Give the position of every malaria parasite and every leukocyte.
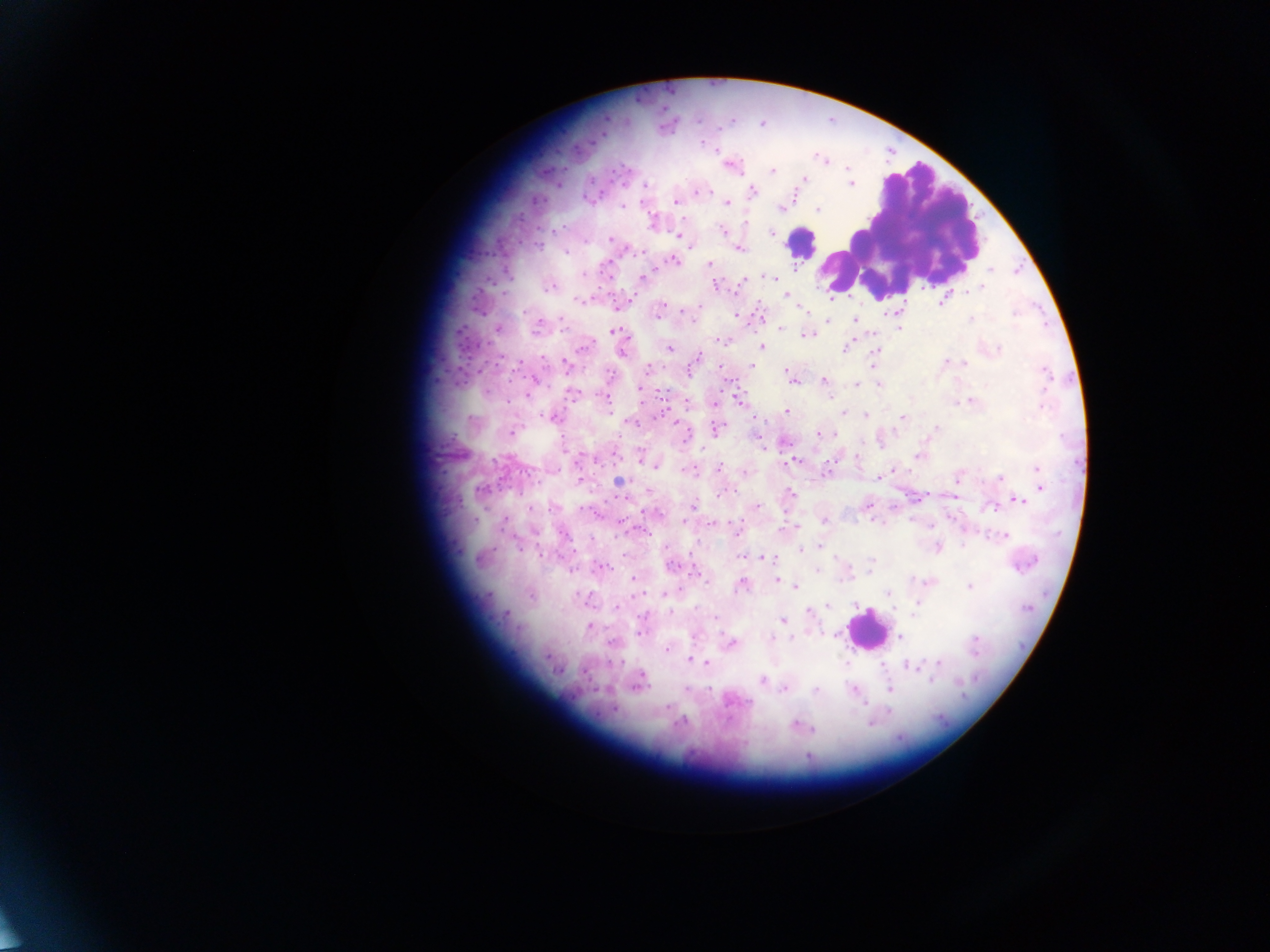

Approximate centers as (x, y) in pixels.
Malaria parasites: (701, 143), (822, 159), (731, 166), (847, 168), (772, 170), (805, 178), (852, 184), (646, 186), (752, 190), (701, 191), (675, 201), (728, 203), (622, 207), (780, 208), (818, 210), (723, 230), (771, 233), (678, 235), (610, 239), (739, 248), (566, 253), (674, 261), (709, 264), (990, 270), (583, 275), (774, 277), (642, 278), (745, 278), (741, 283), (716, 285), (550, 287), (982, 287), (963, 291), (786, 295), (830, 296), (579, 300), (943, 302), (698, 307), (802, 308), (525, 311), (682, 312), (1014, 314), (658, 315), (736, 316), (561, 319), (828, 320), (855, 320), (971, 320), (497, 329), (537, 329), (781, 329), (900, 329), (613, 331), (806, 334), (720, 341), (583, 347), (762, 347), (846, 348), (670, 349), (998, 349), (876, 351), (623, 353), (697, 358), (946, 361), (965, 363), (567, 365), (871, 365), (751, 366), (720, 367), (691, 368), (648, 369), (785, 370), (1044, 372), (824, 380), (793, 381), (857, 384), (878, 385), (640, 389), (572, 393), (528, 395), (830, 397), (737, 398), (971, 400), (961, 401), (956, 402), (608, 403), (1042, 406), (787, 411), (844, 413), (866, 415), (551, 417), (902, 418), (630, 422), (936, 427), (716, 428), (512, 433), (819, 435), (687, 437), (758, 437), (864, 442), (917, 457), (856, 458), (832, 460), (794, 461), (654, 466), (719, 468), (1037, 469), (688, 470), (745, 471), (1000, 477), (878, 478), (958, 478), (618, 482), (1040, 488), (481, 490), (721, 493), (791, 494), (956, 496), (1019, 500), (693, 505), (756, 506), (867, 506), (530, 508), (995, 508), (824, 521), (871, 521), (712, 524), (795, 526), (736, 527), (564, 534), (646, 534), (1004, 536), (963, 545), (820, 546), (937, 547), (800, 549), (741, 557), (769, 558), (871, 562), (602, 566), (669, 566), (694, 571), (817, 571), (870, 572), (633, 579), (845, 579), (707, 580), (777, 580), (741, 586), (796, 587), (970, 587), (886, 593), (664, 594), (917, 604), (828, 605), (916, 607), (616, 608), (696, 608), (893, 609), (809, 612), (671, 613), (507, 614), (783, 620), (589, 627), (640, 633), (694, 636), (901, 636), (790, 637), (771, 638), (974, 639), (610, 643), (732, 643), (666, 649), (974, 651), (688, 659), (846, 663), (939, 663), (706, 664), (912, 666), (762, 680), (932, 680), (638, 685), (710, 688), (686, 689), (784, 689), (854, 689), (889, 690), (816, 691), (667, 707), (888, 710), (870, 723), (794, 725), (814, 729).
Leukocytes: (899, 227), (803, 242), (865, 630).

Summary:
  - Country: Ghana
  - Capture: mobile-phone photograph through a microscope
  - Preparation: thick blood film
  - Image size: 1270×952 pixels
  - Field of view: single